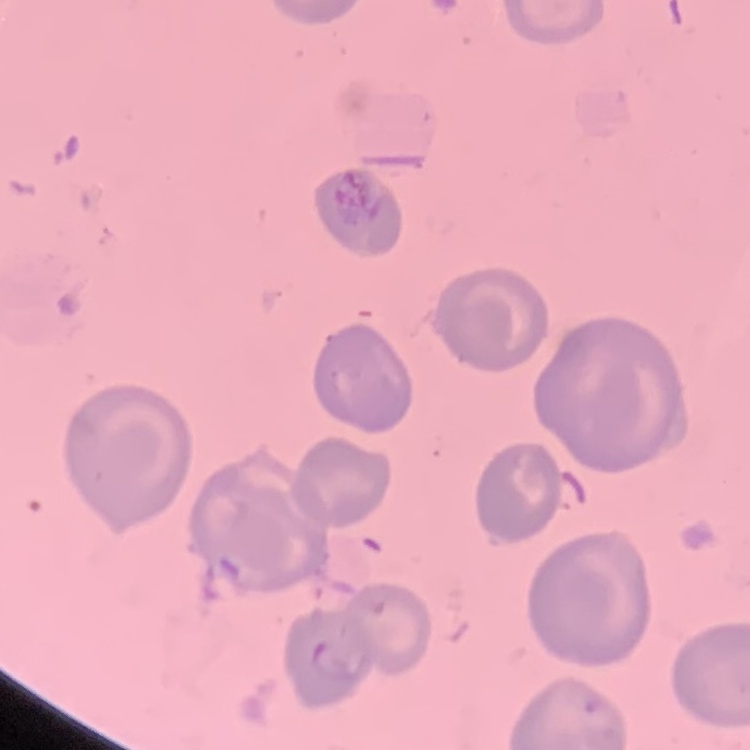
The red blood cells exhibit no rouleaux formation. Thin blood film. Square crop of a larger photomicrograph. Field's or Giemsa stain.